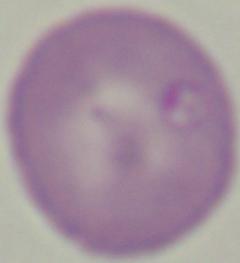
Micrograph. Captured at 1000x magnification. A Babesia parasite is shown.